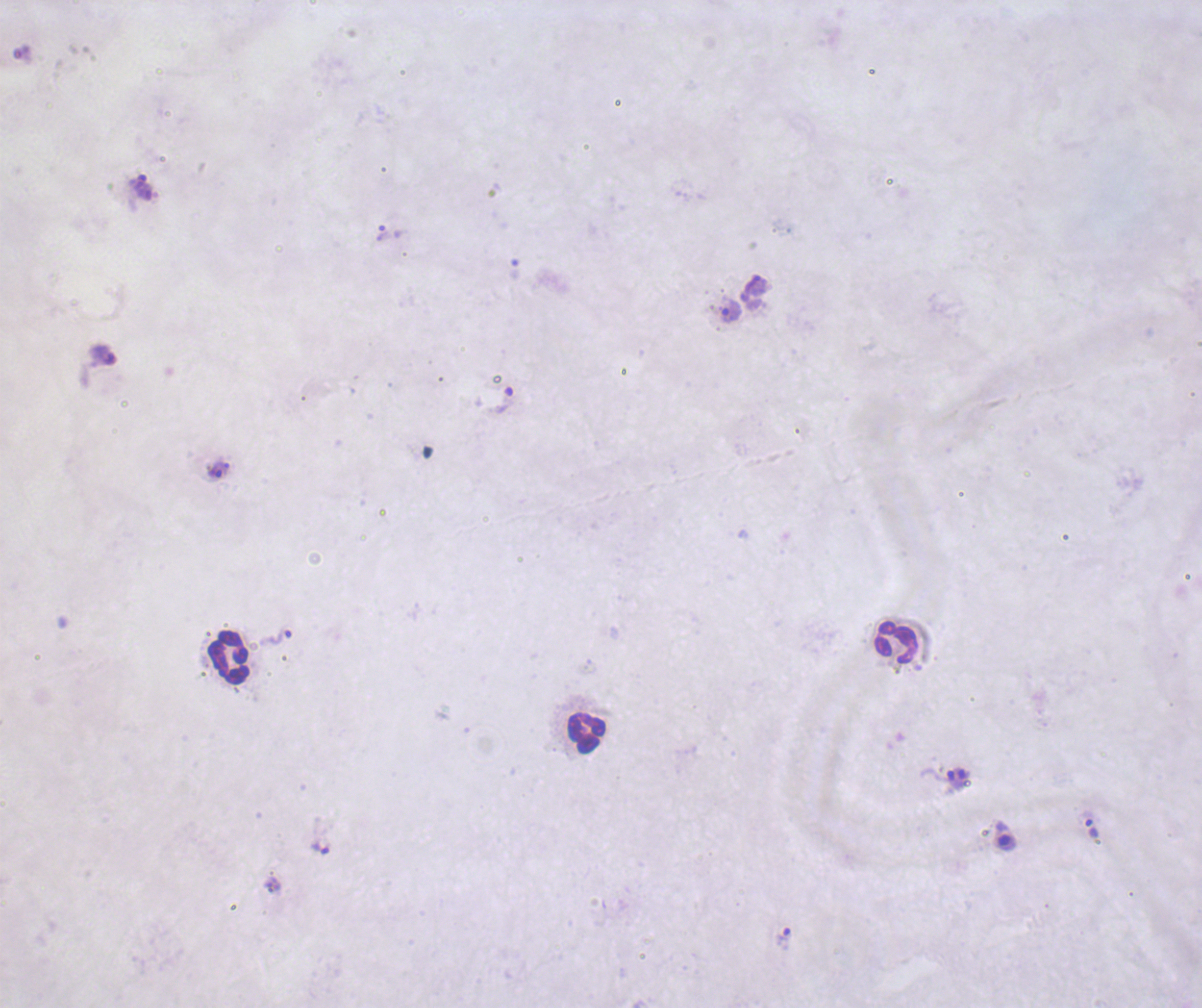

Approximate object centers, in pixels from the top-left corner. Trophozoite locations: (x=137, y=181), (x=383, y=233), (x=731, y=311), (x=506, y=400), (x=224, y=467), (x=215, y=472), (x=280, y=636), (x=1092, y=828), (x=321, y=848), (x=783, y=939). Gametocyte locations: (x=1005, y=841). Leukocyte locations: (x=897, y=642), (x=228, y=657), (x=587, y=733). Life-cycle stages observed: trophozoite, gametocyte. Background quality: poor. Thick smear of blood. Romanowsky stain. One field from this slide. Coloration quality: bad. Image is 1202×1008 pixels. 100x magnification. Result: malaria parasites identified. Previously used in a real diagnosis.